Assess this cell for malaria.
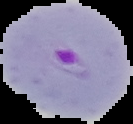

It is parasitized.

Summary:
  - Image size: 133×124 pixels
  - Image type: segmented cell region with the area outside set to black
  - Preparation: thin blood smear